Comment on the morphology of the red blood cells.
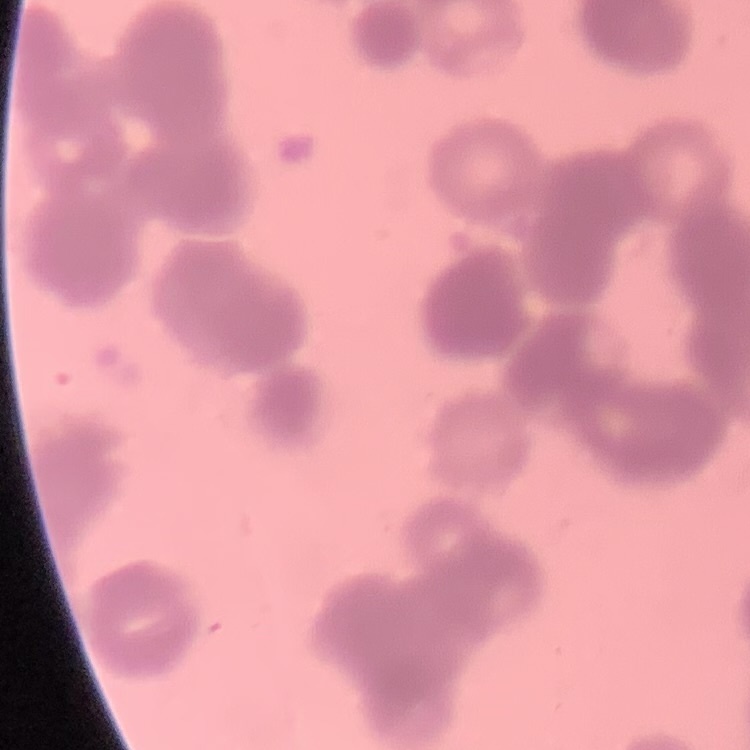
They show rouleaux formation.

Summary:
  - Stain: Field's or Giemsa
  - Preparation: thin blood film
  - Image type: square crop of a larger photomicrograph